Assess this cell for malaria.
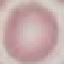

It is uninfected.

Photographed with a smartphone camera at the microscope eyepiece. Automatically extracted cell patch, resized to 64 × 64 pixels. Thin blood film. Giemsa-stained preparation.